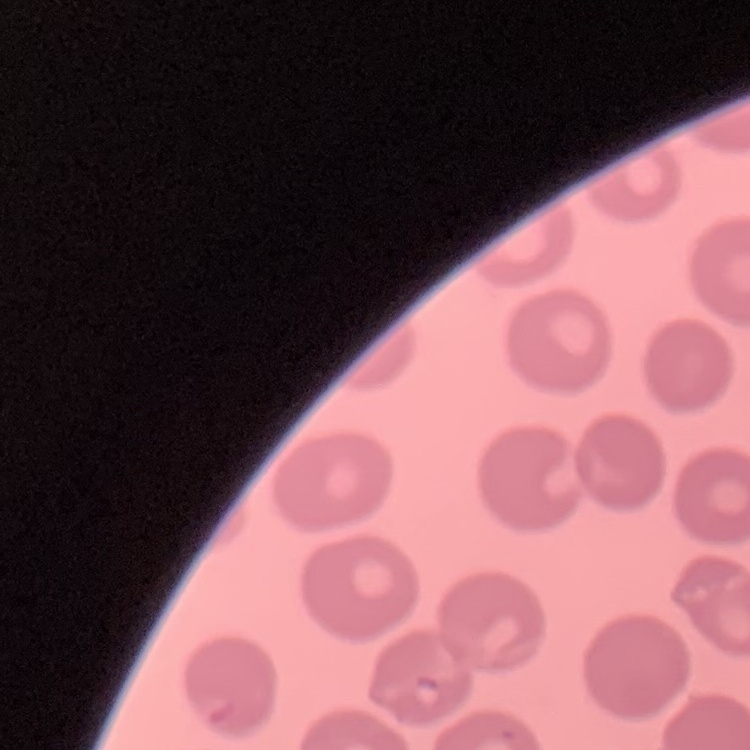
Summary:
  - Erythrocyte morphology: no rouleaux formation
  - Preparation: thin peripheral smear
  - Stain: Field's or Giemsa
  - Image type: one tile cut from a larger photomicrograph